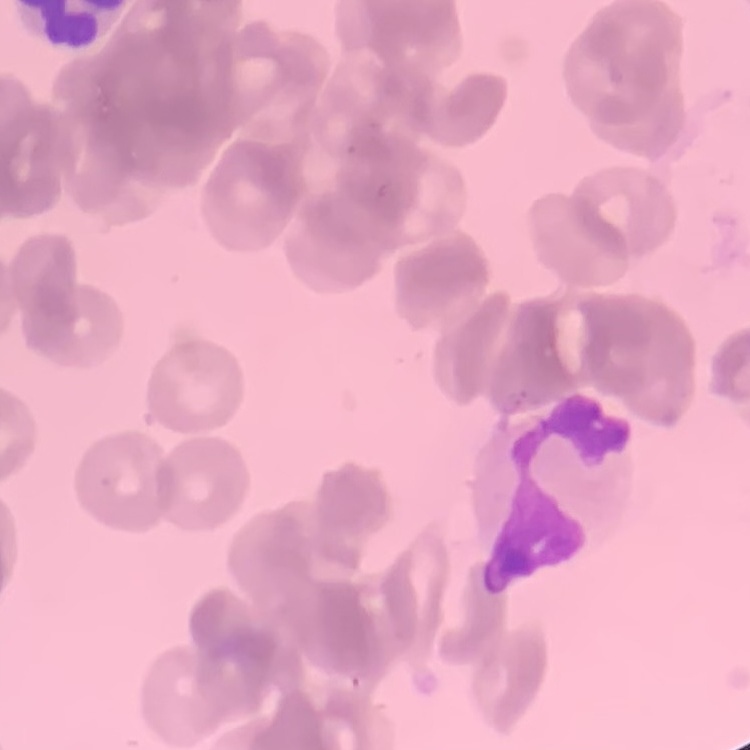 The red blood cells exhibit rouleaux formation. One tile cut from a larger photomicrograph. Field's or Giemsa stain. Thin peripheral smear.